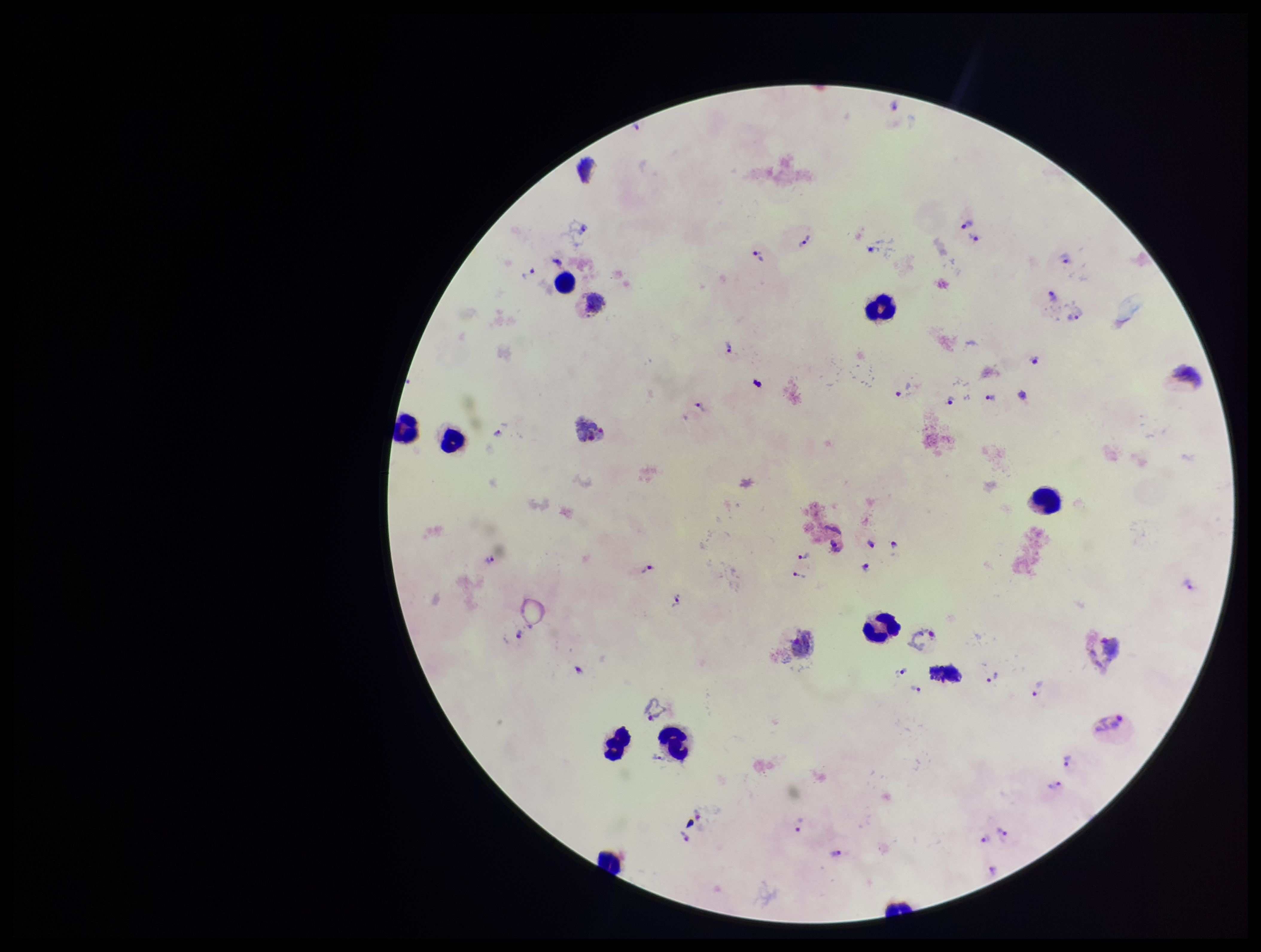 Plasmodium parasites: detected. Patient malaria status: infected. Leukocyte count: 10. Parasite count: 40. Image is 1261×952 pixels. Photographed through the microscope eyepiece with a smartphone camera. Preparation: thick. Stained with Giemsa. Single field of view. Species reported for this patient: Plasmodium vivax.